Identify the parasite.
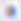
Toxoplasma gondii.

modality: photomicrograph
magnification: 400x